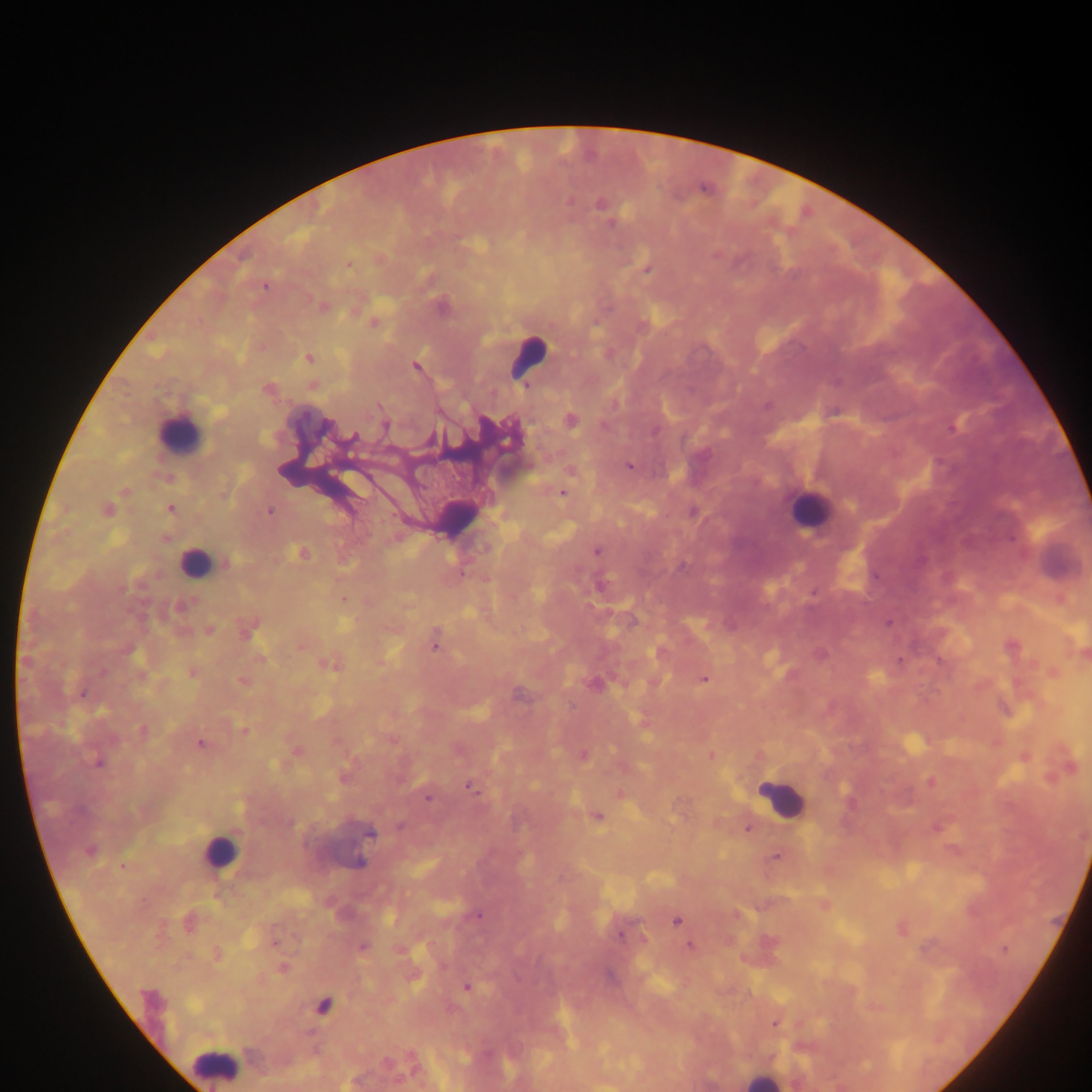
Approximate centers as (x, y) in pixels. Malaria parasite locations: (600, 204), (611, 224), (348, 265), (647, 269), (265, 287), (322, 306), (442, 306), (374, 324), (309, 359), (416, 367), (267, 389), (767, 405), (570, 420), (386, 426), (954, 426), (326, 428), (656, 431), (352, 438), (510, 439), (629, 465), (570, 471), (126, 491), (562, 493), (170, 508), (108, 509), (269, 511), (692, 512), (596, 551), (302, 553), (227, 564), (462, 573), (601, 585), (813, 593), (343, 599), (180, 607), (889, 623), (209, 629), (248, 631), (435, 647), (133, 652), (900, 661), (329, 664), (192, 673), (704, 679), (243, 682), (594, 684), (82, 694), (142, 730), (245, 730), (201, 743), (584, 755), (711, 757), (98, 763), (470, 787), (426, 798), (598, 818), (400, 825), (747, 829), (369, 833), (90, 851), (776, 857), (360, 863), (123, 866), (478, 915), (676, 921), (188, 923), (621, 936), (275, 941), (690, 946), (363, 947), (1004, 949), (217, 954), (284, 967), (609, 977), (467, 987), (150, 998), (323, 1006), (775, 1023). Leukocyte locations: (526, 357), (179, 433), (809, 508), (456, 514), (194, 562), (781, 800), (220, 853), (215, 1065), (763, 1080). Image is 1092×1092 pixels. One field of view. Sample from Ghana. Thick blood smear. Mobile-phone photograph taken through the microscope.